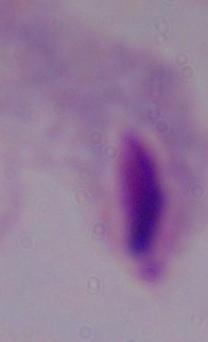 Photomicrograph. Captured at 1000x magnification. A trichomonad is seen.